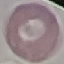
{
  "malaria_status": "uninfected",
  "stain": "Giemsa",
  "preparation": "thin smear",
  "image_type": "cell patch, automatically extracted from a larger field of view and resized to 64 × 64 pixels",
  "capture": "smartphone camera at the microscope eyepiece"
}